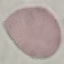

Result: no malaria parasites detected. Giemsa-stained preparation. Acquired by smartphone through the microscope eyepiece. Thin smear of blood. Automatically extracted cell patch, resized to 64 × 64 pixels.